Identify the parasite.
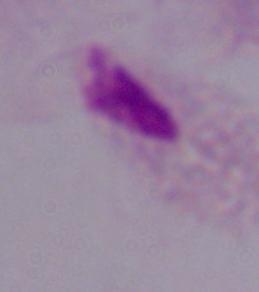
This is a trichomonad.

Summary:
  - Magnification: 1000x
  - Modality: photomicrograph